Identify the parasite.
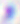
This is Toxoplasma gondii.

Captured at 400x magnification. Micrograph.